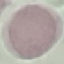
malaria status = uninfected
stain = Giemsa
image type = cell patch, automatically extracted from a larger field of view and resized to 64 × 64 pixels
preparation = thin blood smear
capture = smartphone camera at the microscope eyepiece